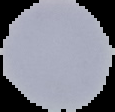

Image is 115×112 pixels. Malaria status: uninfected. From a thin blood smear. Cell region segmented out of the field of view; the surrounding area is masked to black.